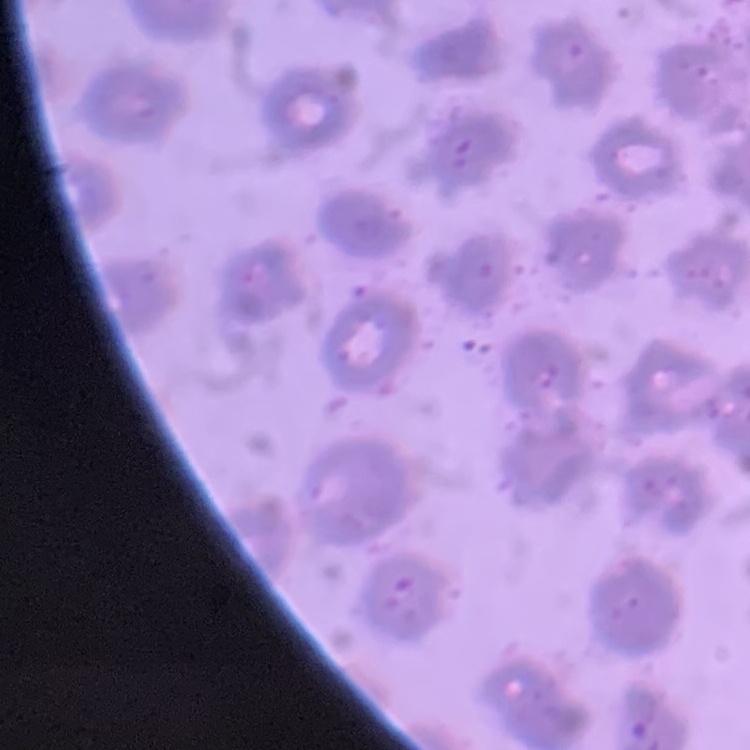
erythrocyte morphology = no rouleaux formation
stain = Field's or Giemsa
image type = square crop of a larger photomicrograph
preparation = thin blood smear